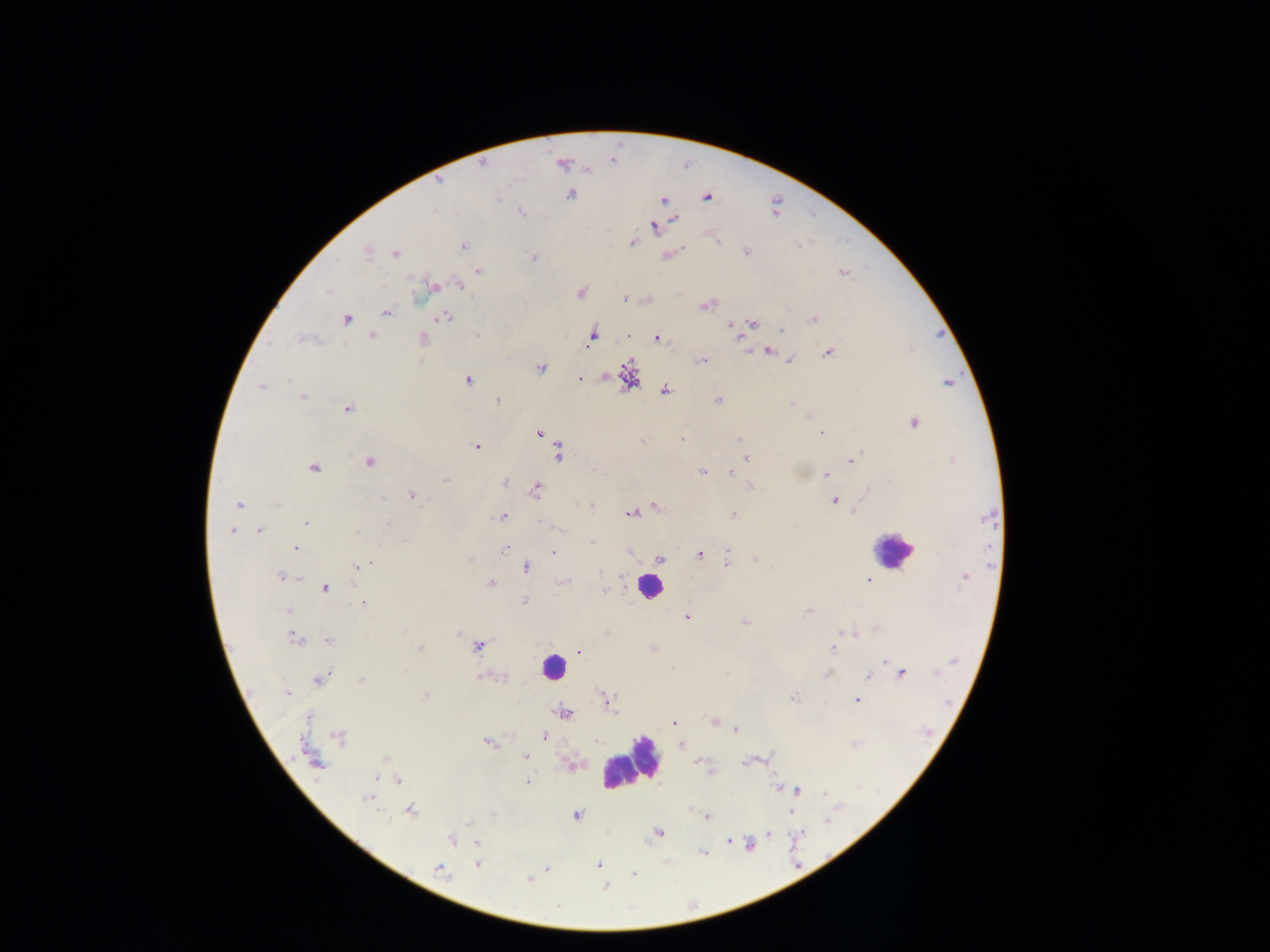

preparation: thick blood film
country: Ghana
field_of_view: single
capture: mobile-phone photograph through a microscope
plasmodium_parasite_locations: 'approximate centers as {x, y} in pixels: {562, 163}, {482, 164}, {571, 194}, {707, 196}, {664, 200}, {521, 211}, {675, 219}, {654, 226}, {717, 240}, {632, 242}, {462, 246}, {745, 250}, {367, 251}, {395, 252}, {668, 255}, {534, 257}, {478, 270}, {842, 273}, {459, 284}, {431, 286}, {580, 292}, {624, 298}, {648, 299}, {707, 303}, {385, 312}, {445, 316}, {345, 318}, {812, 320}, {730, 323}, {752, 323}, {780, 331}, {372, 336}, {592, 336}, {629, 336}, {739, 336}, {656, 337}, {302, 339}, {422, 339}, {768, 350}, {828, 351}, {701, 359}, {790, 361}, {541, 368}, {628, 376}, {579, 378}, {467, 379}, {948, 383}, {262, 386}, {664, 390}, {302, 397}, {717, 400}, {497, 401}, {347, 407}, {913, 422}, {538, 433}, {822, 433}, {681, 438}, {739, 439}, {477, 447}, {559, 452}, {747, 457}, {851, 460}, {369, 462}, {313, 467}, {702, 471}, {731, 471}, {826, 474}, {447, 480}, {504, 482}, {749, 487}, {535, 489}, {412, 495}, {834, 500}, {590, 503}, {239, 504}, {655, 507}, {631, 512}, {853, 512}, {732, 515}, {503, 516}, {988, 517}, {306, 523}, {231, 530}, {258, 530}, {591, 543}, {505, 548}, {294, 549}, {552, 551}, {700, 553}, {659, 558}, {470, 559}, {755, 559}, {726, 565}, {357, 566}, {526, 567}, {281, 576}, {964, 576}, {868, 581}, {563, 582}, {490, 583}, {324, 588}, {604, 591}, {525, 600}, {364, 602}, {289, 610}, {808, 611}, {686, 616}, {744, 622}, {606, 632}, {293, 637}, {328, 640}, {478, 645}, {833, 647}, {419, 648}, {653, 648}, {578, 650}, {884, 661}, {901, 673}, {827, 674}, {484, 676}, {501, 676}, {867, 677}, {319, 679}, {361, 679}, {287, 692}, {424, 696}, {792, 698}, {606, 700}, {856, 700}, {564, 713}, {673, 723}, {714, 723}, {735, 729}, {543, 736}, {340, 738}, {487, 742}, {680, 744}, {526, 757}, {385, 759}, {699, 760}, {748, 760}, {315, 762}, {573, 765}, {710, 772}, {397, 779}, {527, 782}, {780, 788}, {797, 790}, {369, 798}, {410, 810}, {790, 812}, {575, 815}, {707, 817}, {658, 832}, {767, 834}, {452, 840}, {728, 841}, {478, 843}, {749, 844}, {702, 852}, {477, 864}, {598, 864}, {546, 868}, {439, 870}, {633, 875}, {528, 879}, {605, 886}'
image_size: 1270×952 pixels
leukocyte_locations: 'approximate centers as {x, y} in pixels: {892, 549}, {649, 585}, {553, 667}, {629, 762}'